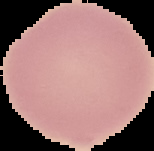

Image is 154×151 pixels. From a thin blood smear. Malaria status: uninfected. The area outside the segmented cell region is set to black.